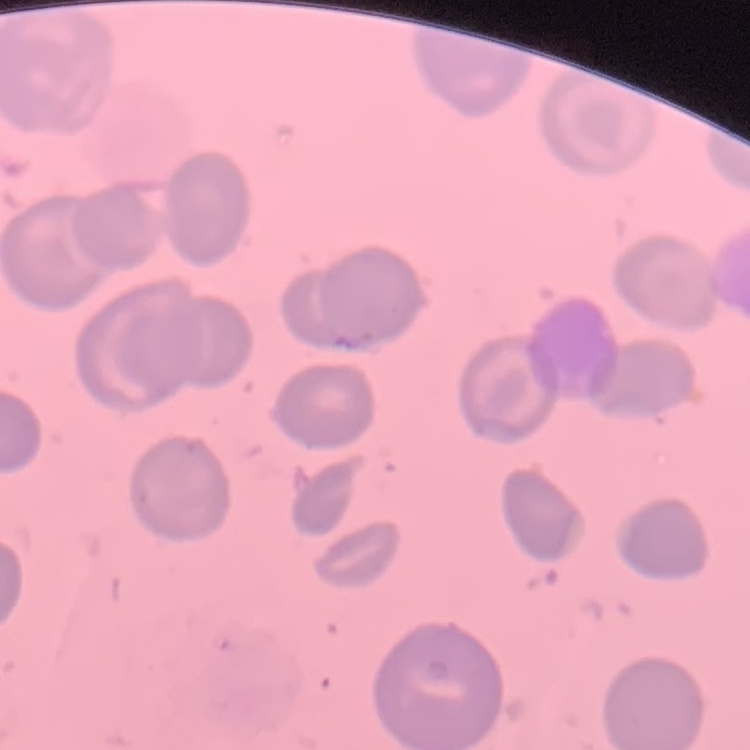

Summary:
  - Red blood cell morphology: no rouleaux formation
  - Preparation: thin blood film
  - Stain: Field's or Giemsa
  - Image type: one tile cut from a larger photomicrograph